Locate and identify every blood parasite.
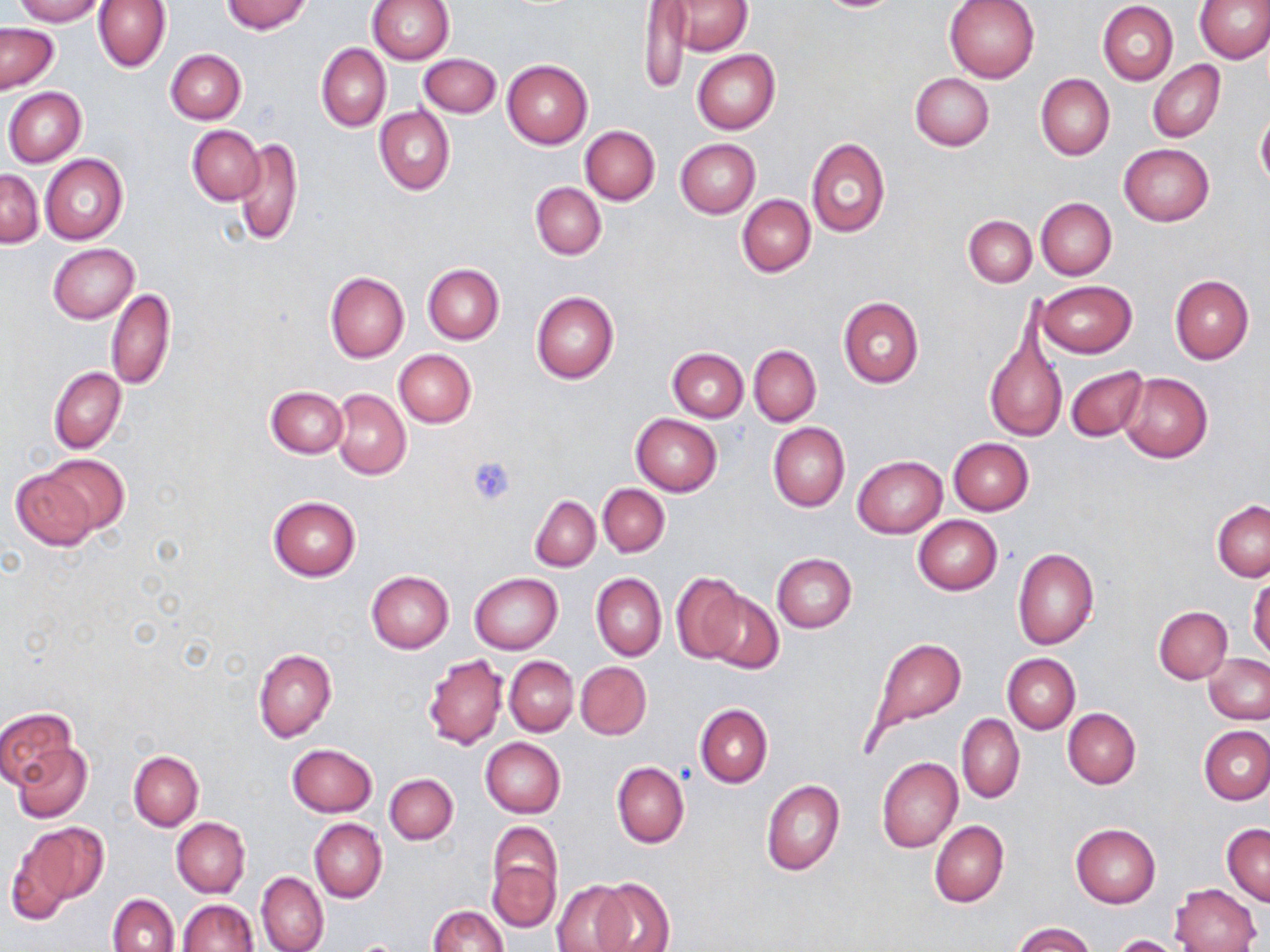
No blood parasites seen.

Approximate bounding boxes as (x1, y1, x2, y2) in pixels. Uninfected red blood cell locations: (12, 0, 104, 25), (94, 0, 170, 72), (222, 0, 312, 34), (367, 0, 453, 63), (944, 0, 1041, 83), (1196, 0, 1270, 63), (667, 1, 752, 55), (1098, 2, 1178, 84), (638, 4, 691, 96), (1, 23, 59, 93), (316, 43, 390, 131), (165, 49, 245, 124), (692, 49, 780, 134), (418, 54, 501, 118), (501, 58, 593, 149), (1147, 60, 1225, 142), (910, 73, 994, 151), (1035, 74, 1113, 159), (4, 87, 86, 166), (375, 106, 454, 196), (1255, 108, 1270, 188), (187, 124, 265, 205), (580, 126, 659, 204), (233, 135, 303, 247), (806, 138, 889, 237), (675, 139, 759, 218), (1118, 143, 1215, 226), (40, 154, 128, 245), (1, 171, 44, 247), (530, 181, 605, 259), (737, 194, 816, 277), (1036, 197, 1116, 279), (964, 215, 1036, 287), (48, 244, 138, 323), (423, 264, 504, 344), (325, 272, 409, 362), (1169, 275, 1253, 365), (1039, 281, 1137, 357), (105, 288, 175, 389), (531, 291, 618, 384), (837, 297, 924, 388), (984, 326, 1066, 444), (749, 344, 821, 427), (667, 346, 748, 421), (392, 349, 476, 427), (1066, 365, 1146, 442), (49, 367, 126, 452), (1117, 371, 1213, 463), (266, 386, 348, 458), (331, 388, 411, 480), (631, 413, 723, 495), (768, 422, 849, 512), (947, 438, 1033, 516), (41, 454, 128, 535), (852, 455, 946, 538), (11, 469, 98, 550), (598, 484, 669, 557), (530, 495, 600, 571), (268, 496, 360, 580), (1212, 501, 1269, 581), (912, 516, 1001, 595), (1012, 547, 1099, 649), (771, 553, 856, 632), (365, 571, 454, 653), (469, 572, 563, 654), (592, 573, 666, 661), (672, 573, 747, 662), (1248, 575, 1269, 658), (701, 589, 783, 674), (1154, 606, 1233, 684), (867, 637, 968, 743), (253, 648, 336, 742), (423, 654, 508, 750), (1002, 654, 1080, 733), (1204, 654, 1270, 724), (505, 657, 577, 735), (576, 661, 651, 739), (695, 703, 772, 787), (0, 708, 76, 789), (1063, 709, 1140, 789), (957, 713, 1024, 802), (1200, 727, 1270, 804), (480, 737, 566, 818), (13, 743, 92, 823), (287, 743, 377, 817), (129, 750, 203, 830), (877, 757, 963, 853), (611, 761, 690, 847), (385, 772, 458, 845), (761, 780, 844, 877), (171, 817, 250, 897), (309, 819, 386, 903), (929, 820, 1009, 907), (17, 821, 109, 908), (1222, 822, 1269, 905), (1070, 823, 1160, 908), (487, 828, 562, 930), (5, 842, 76, 924), (256, 872, 328, 952), (552, 879, 634, 952), (593, 879, 674, 952), (1170, 884, 1260, 952), (107, 893, 178, 952), (178, 900, 257, 952), (429, 905, 507, 952), (1011, 923, 1095, 952), (1109, 934, 1184, 952). Platelet locations: (468, 456, 516, 507). Slide-level diagnosis: negative for blood parasites. Single field of view. Light microscopy. Image is 1270×952 pixels. Thin blood smear. 1000x magnification. May-Grünwald-Giemsa stain.